Report the malaria status of this cell.
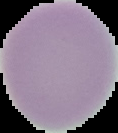
It is uninfected.

Summary:
  - Image size: 118×133 pixels
  - Image type: cell region segmented out of the field of view; surrounding area masked to black
  - Preparation: thin blood smear